Assess the morphology of the erythrocytes.
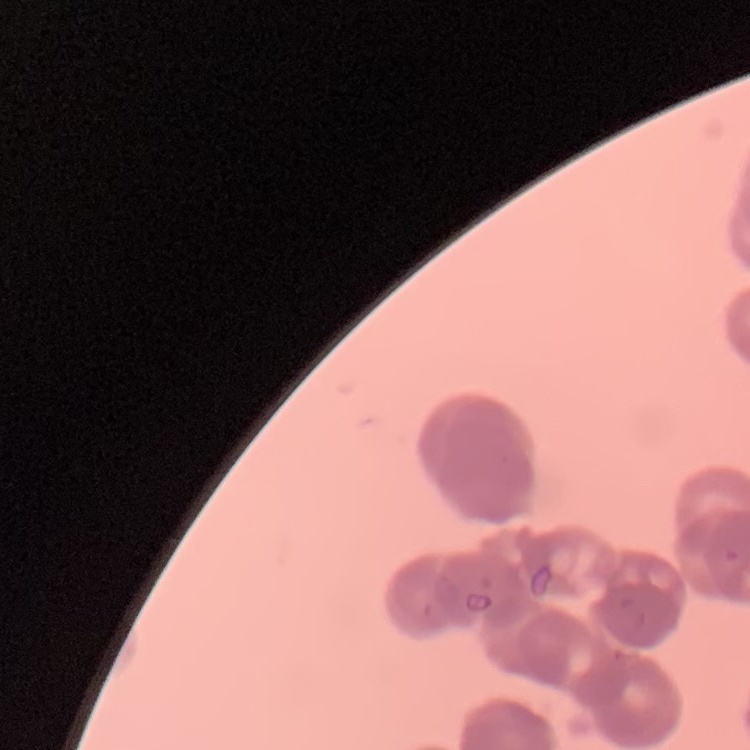
They show rouleaux formation.

preparation = thin blood smear
image type = square crop of a larger photomicrograph
stain = Field's or Giemsa